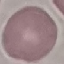

{
  "malaria_status": "uninfected",
  "capture": "smartphone camera at the microscope eyepiece",
  "image_type": "cell patch, automatically extracted from a larger field of view and resized to 64 × 64 pixels",
  "stain": "Giemsa",
  "preparation": "thin smear"
}